Assess this cell for malaria.
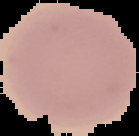

Uninfected.

image size = 139×136 pixels
image type = segmented cell region with the area outside set to black
preparation = thin blood film